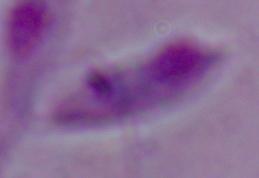
magnification = 1000x
identification = Leishmania
modality = micrograph